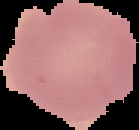

{
  "image_size": "139×130 pixels",
  "image_type": "segmented cell region with the area outside set to black",
  "preparation": "thin blood smear",
  "malaria_status": "uninfected"
}